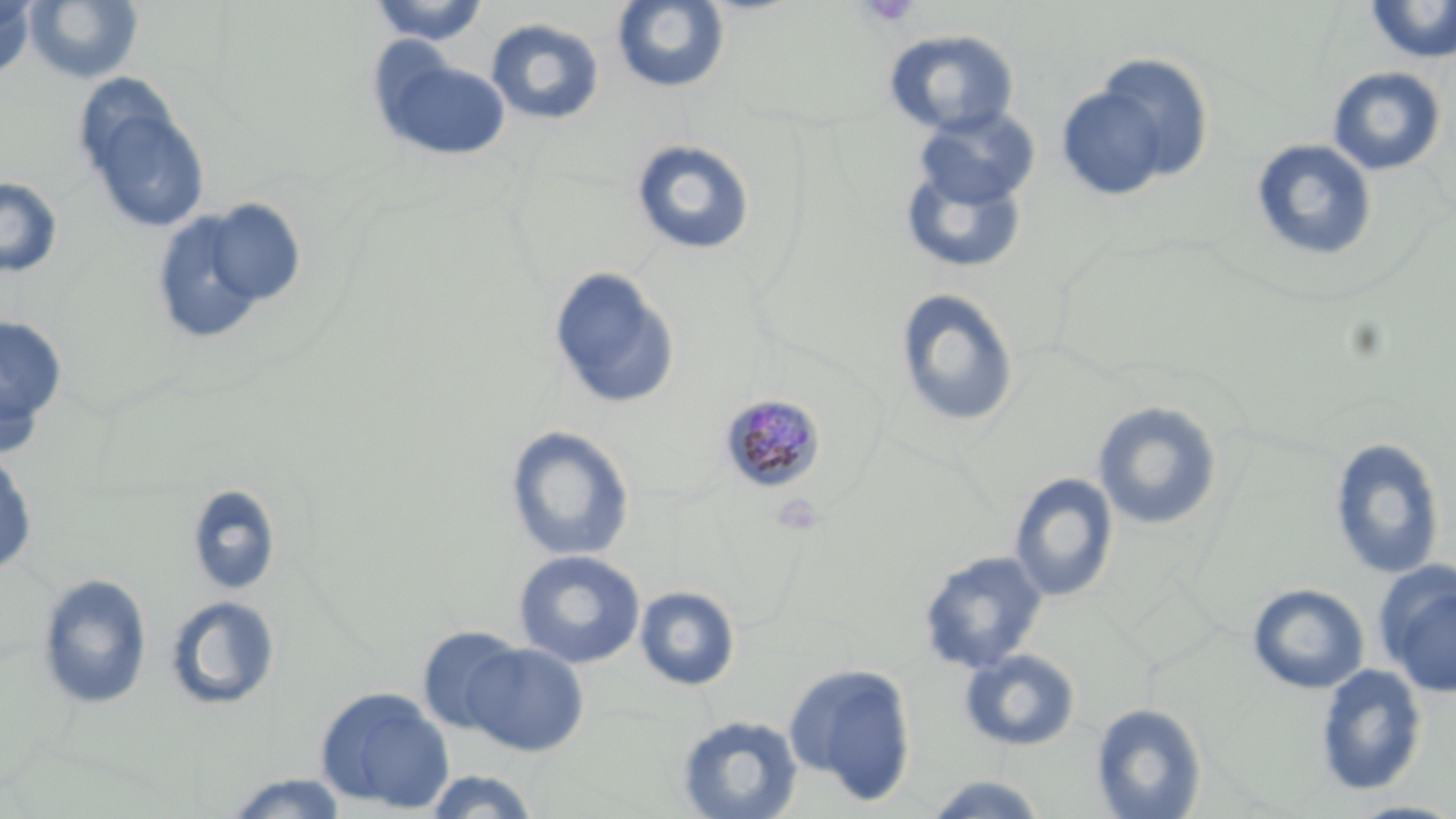
{
  "slide_level_diagnosis": "Plasmodium malariae",
  "uninfected_red_blood_cell_locations": "approximate bounding boxes as [x1, y1, x2, y2] in pixels: [24, 0, 144, 84], [367, 0, 490, 46], [611, 0, 730, 95], [0, 1, 37, 78], [1364, 1, 1456, 64], [485, 18, 606, 127], [883, 28, 1022, 139], [372, 53, 511, 162], [1059, 62, 1206, 197], [1327, 66, 1447, 177], [73, 81, 211, 236], [913, 106, 1040, 210], [629, 138, 756, 256], [1250, 139, 1379, 264], [898, 156, 1029, 276], [0, 176, 63, 278], [149, 199, 298, 341], [547, 266, 681, 411], [894, 288, 1020, 429], [0, 316, 67, 443], [1093, 402, 1223, 532], [505, 425, 635, 563], [1329, 437, 1445, 580], [0, 450, 37, 576], [1008, 472, 1119, 604], [186, 484, 281, 596], [512, 549, 646, 669], [918, 551, 1049, 674], [1374, 562, 1456, 699], [38, 573, 152, 709], [1247, 583, 1369, 695], [634, 585, 741, 691], [165, 595, 280, 711], [416, 626, 530, 738], [457, 640, 589, 757], [957, 647, 1081, 752], [782, 661, 918, 806], [1314, 663, 1427, 798], [315, 686, 455, 814], [1090, 701, 1207, 819], [675, 714, 804, 819], [422, 769, 542, 818], [218, 772, 352, 818], [921, 774, 1051, 818], [1341, 799, 1456, 819]",
  "image_size": "1456×819 pixels",
  "modality": "optical microscopy",
  "magnification": "1000x",
  "platelet_locations": "approximate bounding boxes as [x1, y1, x2, y2] in pixels: [859, 0, 921, 28]",
  "stain": "May-Grünwald-Giemsa",
  "field_of_view": "single",
  "plasmodium_malariae_infected_red_blood_cell_locations": "approximate bounding boxes as [x1, y1, x2, y2] in pixels: [720, 393, 827, 493]",
  "preparation": "thin blood film"
}